Name the parasite shown.
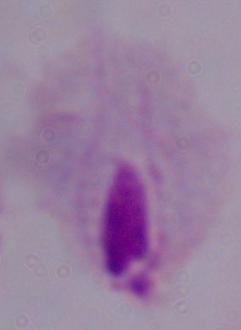
This is a trichomonad.

magnification: 1000x
modality: photomicrograph